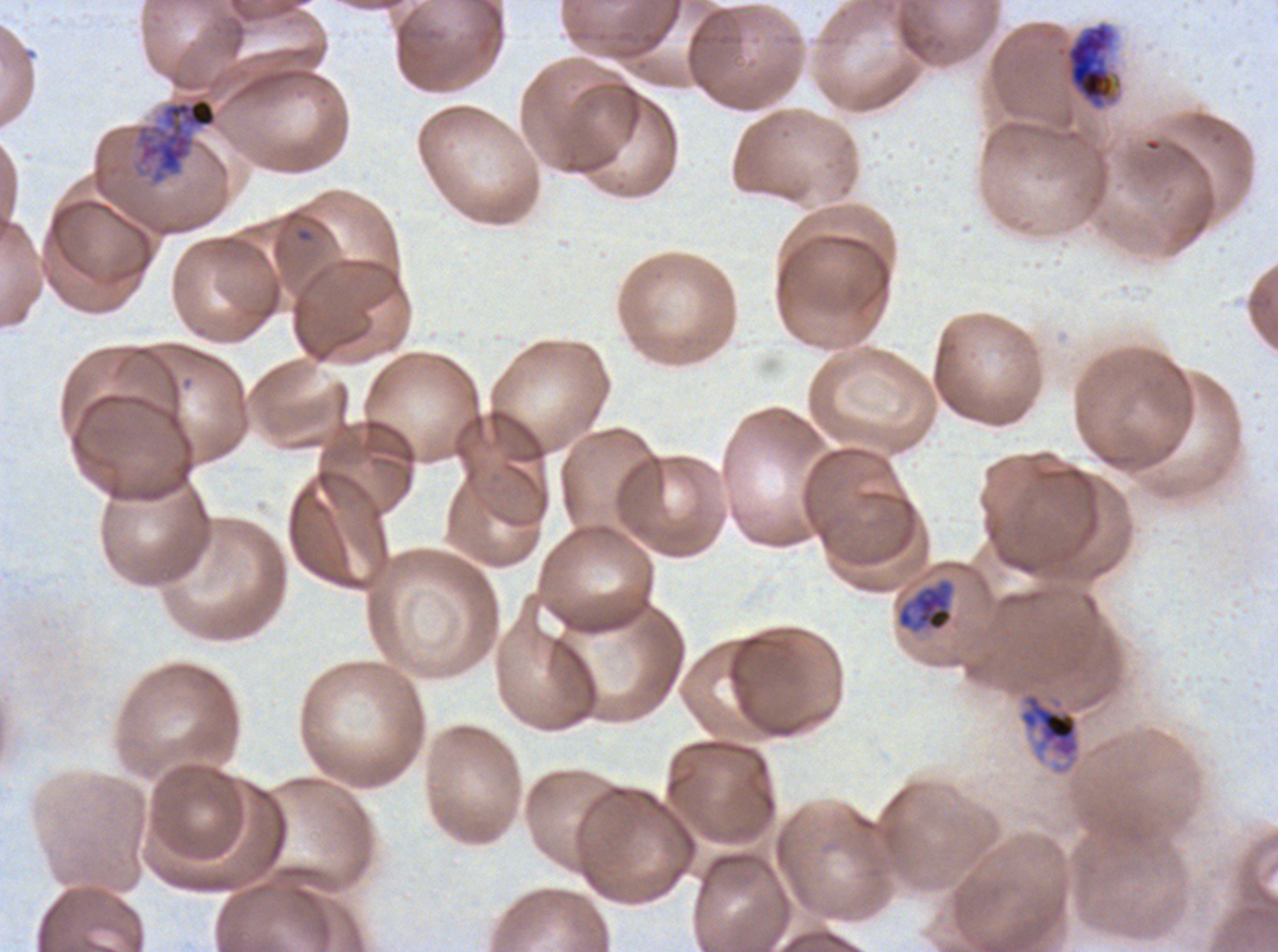

{
  "field_of_view": "one sub-image of a larger composite",
  "late_trophozoite_locations": "approximate bounding boxes as (x1, y1, x2, y2) in pixels: (1054, 20, 1124, 111), (897, 580, 953, 631), (1017, 690, 1082, 775)",
  "image_size": "1278×952 pixels",
  "late_schizont_locations": "approximate bounding boxes as (x1, y1, x2, y2) in pixels: (136, 96, 218, 185)",
  "preparation": "thin blood film",
  "stain": "Giemsa",
  "specimen": "P. falciparum from a patient in The Gambia, cultured ex vivo for 24 to 48 hours",
  "life_cycle_stages_observed": "late trophozoite, late schizont"
}